Assess this cell for malaria.
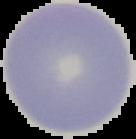

Uninfected.

Summary:
  - Image size: 136×139 pixels
  - Image type: segmented cell region with the area outside set to black
  - Preparation: thin blood film